State which parasite is depicted.
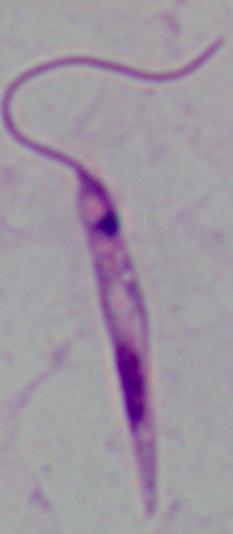

Leishmania.

magnification = 1000x
modality = photomicrograph